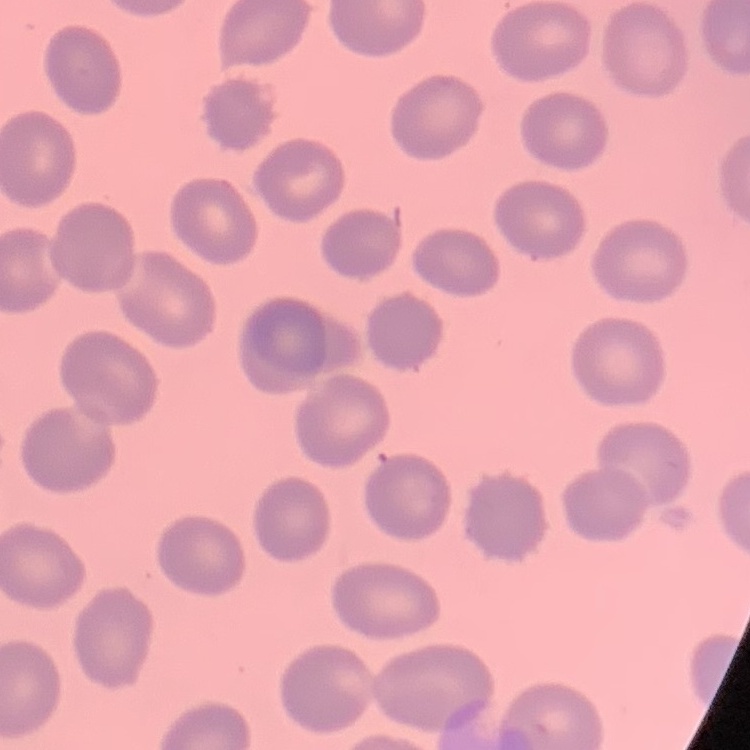
The erythrocytes exhibit no rouleaux formation. Field's or Giemsa stain. Thin peripheral smear. One tile cut from a larger photomicrograph.